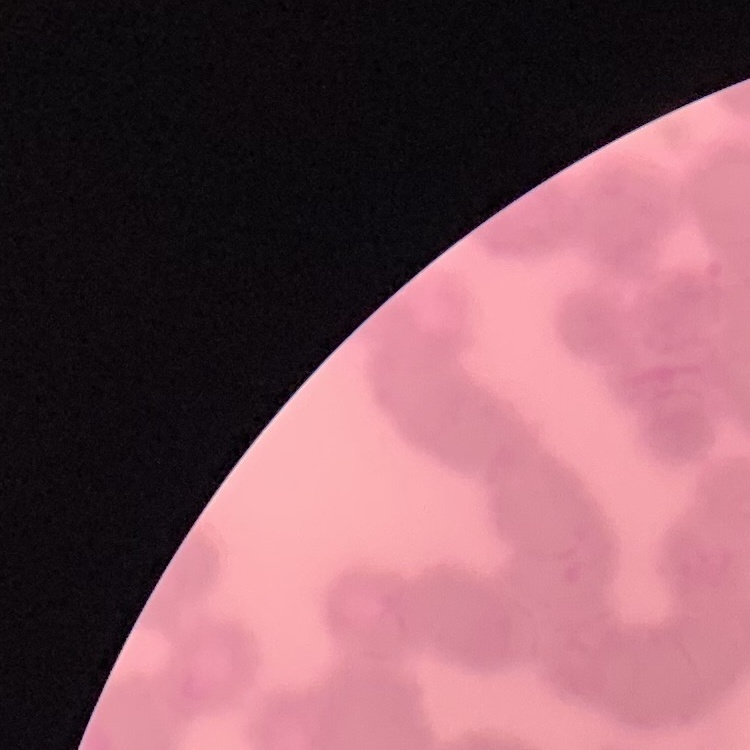
The red blood cells show rouleaux formation. One tile cut from a larger photomicrograph. Thin blood film. Stained with either Field's or Giemsa.